Locate every leukocyte (white blood cell).
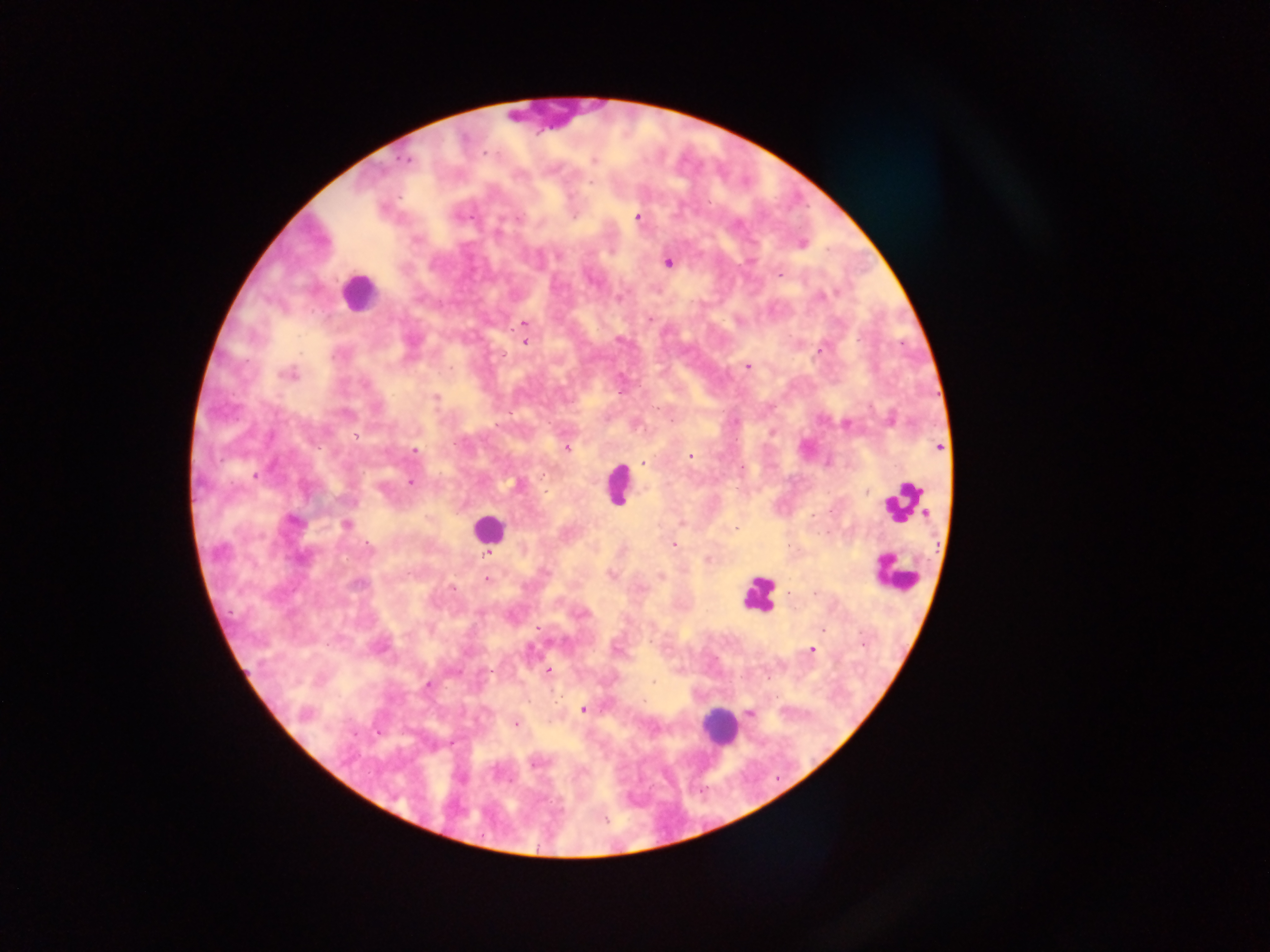
Approximate centers as [x, y] in pixels.
Leukocytes (some below the resolvable threshold): [546, 113], [358, 293], [617, 484], [904, 500], [487, 528], [893, 573], [758, 595], [717, 726].

Plasmodium parasite locations: [406, 160], [594, 160], [399, 196], [638, 217], [519, 218], [418, 239], [801, 244], [558, 255], [668, 263], [779, 276], [836, 293], [829, 294], [821, 295], [650, 319], [524, 323], [619, 340], [525, 343], [820, 349], [503, 355], [747, 367], [450, 368], [288, 374], [436, 397], [891, 419], [846, 424], [356, 436], [939, 447], [568, 448], [415, 451], [690, 455], [643, 463], [255, 475], [411, 482], [518, 484], [867, 491], [293, 521], [346, 525], [735, 529], [673, 545], [487, 554], [709, 561], [611, 574], [662, 577], [487, 579], [358, 584], [452, 587], [641, 587], [538, 628], [823, 629], [616, 649], [812, 650], [490, 671], [548, 671], [455, 672], [653, 682], [428, 685], [583, 709], [750, 713], [304, 714], [516, 723], [536, 762]. Image is 1270×952 pixels. Photographed through a microscope with a mobile-phone camera. One field of view. Sample from Ghana. Thick blood smear.